State which parasite is depicted.
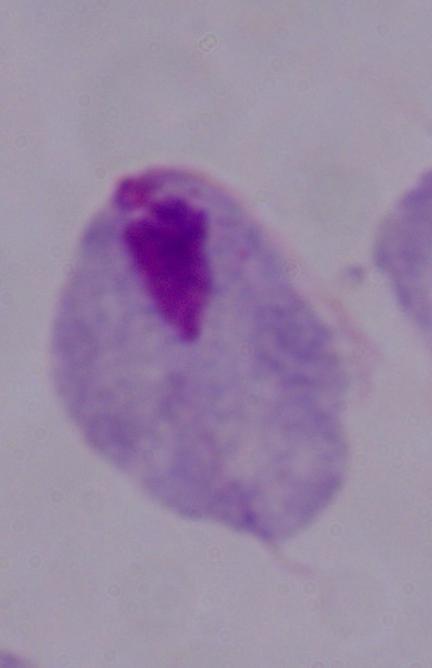

A trichomonad.

Summary:
  - Magnification: 1000x
  - Modality: micrograph